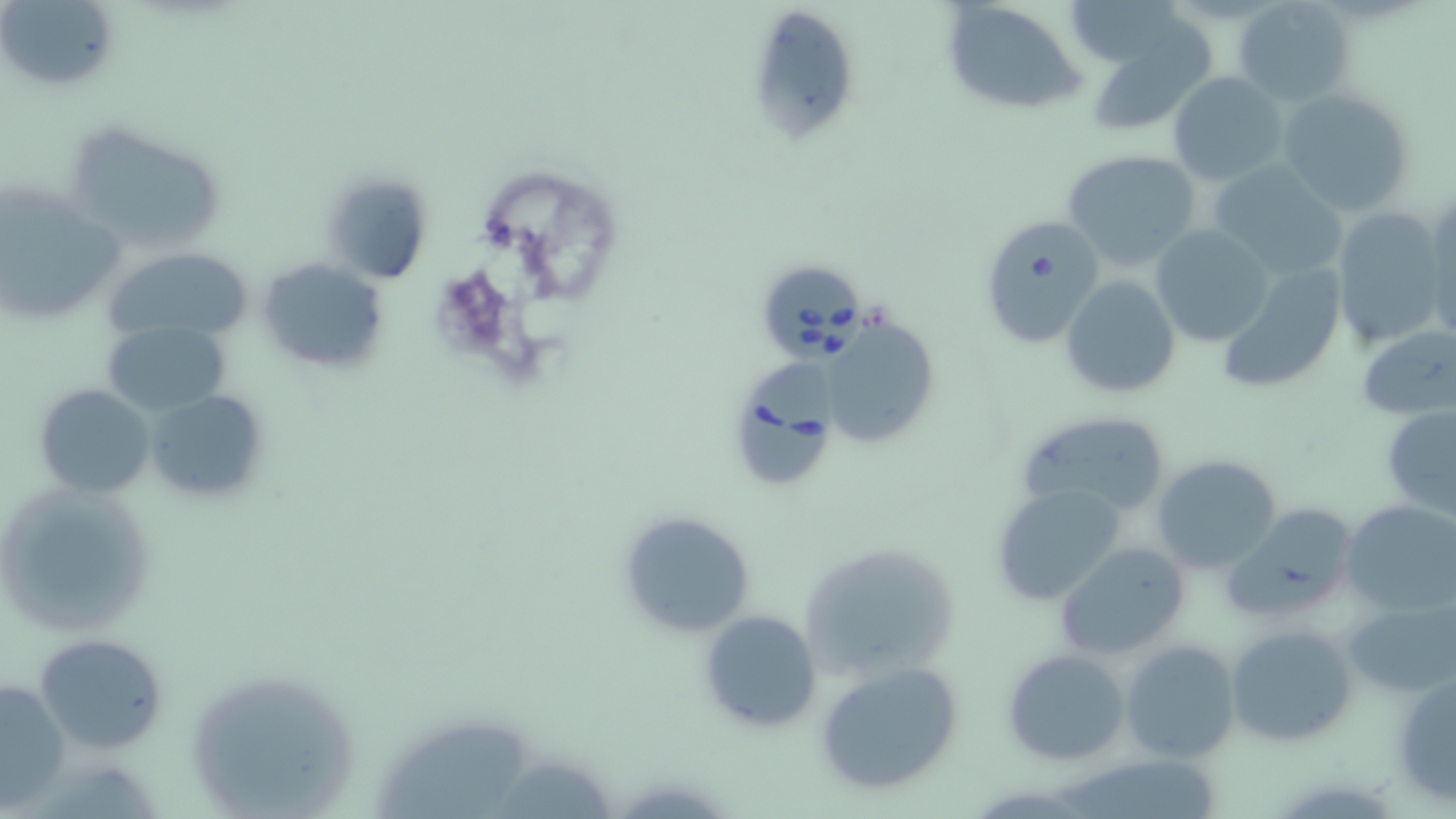
Approximate bounding boxes as (x1, y1, x2, y2) in pixels. Babesia divergens-infected red blood cell locations: (759, 270, 866, 366), (733, 354, 845, 485). Uninfected red blood cell locations: (937, 0, 1087, 117), (3, 1, 121, 94), (1075, 2, 1188, 68), (1233, 2, 1351, 107), (756, 14, 854, 147), (1098, 22, 1215, 130), (1168, 73, 1286, 185), (1277, 87, 1417, 217), (67, 126, 235, 252), (1060, 149, 1204, 272), (1208, 162, 1346, 277), (321, 171, 437, 285), (0, 183, 125, 329), (1425, 193, 1455, 335), (1329, 205, 1449, 349), (978, 218, 1104, 348), (1150, 224, 1273, 345), (102, 245, 256, 348), (255, 256, 389, 378), (1214, 265, 1350, 393), (1060, 273, 1180, 399), (100, 319, 230, 418), (831, 320, 937, 442), (1356, 325, 1456, 420), (33, 382, 159, 499), (144, 387, 269, 505), (1381, 402, 1456, 518), (1016, 410, 1176, 521), (1153, 454, 1284, 574), (0, 479, 162, 640), (990, 482, 1129, 606), (1341, 501, 1456, 616), (1224, 504, 1361, 625), (614, 510, 756, 639), (797, 537, 963, 680), (1053, 542, 1189, 661), (1343, 596, 1455, 699), (696, 610, 821, 733), (1225, 623, 1357, 747), (32, 632, 167, 753), (1121, 639, 1241, 763), (1002, 648, 1131, 766), (814, 662, 966, 797), (1391, 670, 1456, 805), (183, 674, 365, 819), (1, 676, 67, 807), (373, 720, 538, 819). Slide-level diagnosis: Babesia divergens. May-Grünwald-Giemsa stain. Optical microscopy. Image is 1456×819 pixels. Thin blood film. Captured at 1000x magnification. Single field of view.